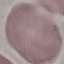
Malaria status: uninfected. Thin blood film. Acquired by smartphone through the microscope eyepiece. Giemsa stain. Automatically extracted cell patch, resized to 64 × 64 pixels.